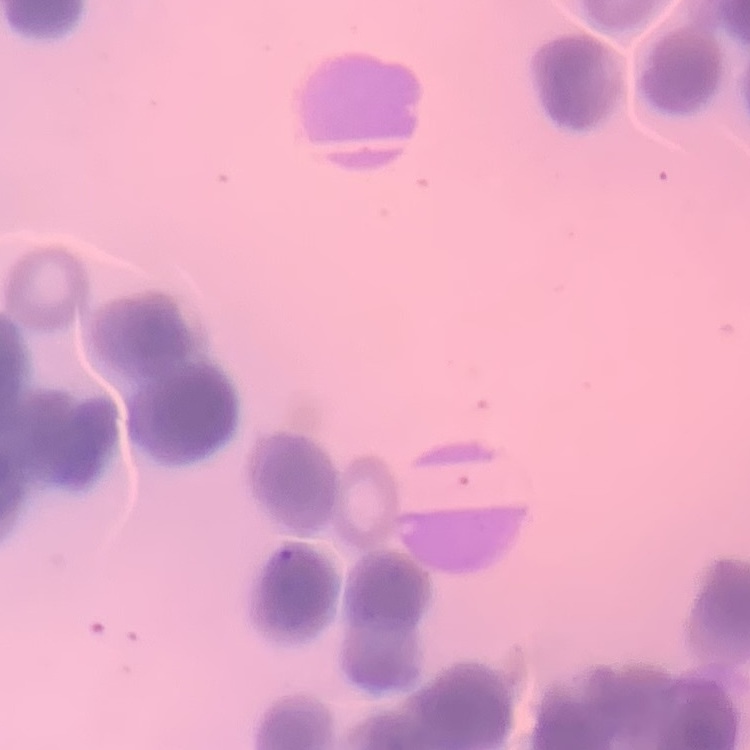 The red blood cells show rouleaux formation. Field's or Giemsa stain. One tile cut from a larger photomicrograph. Thin blood film.